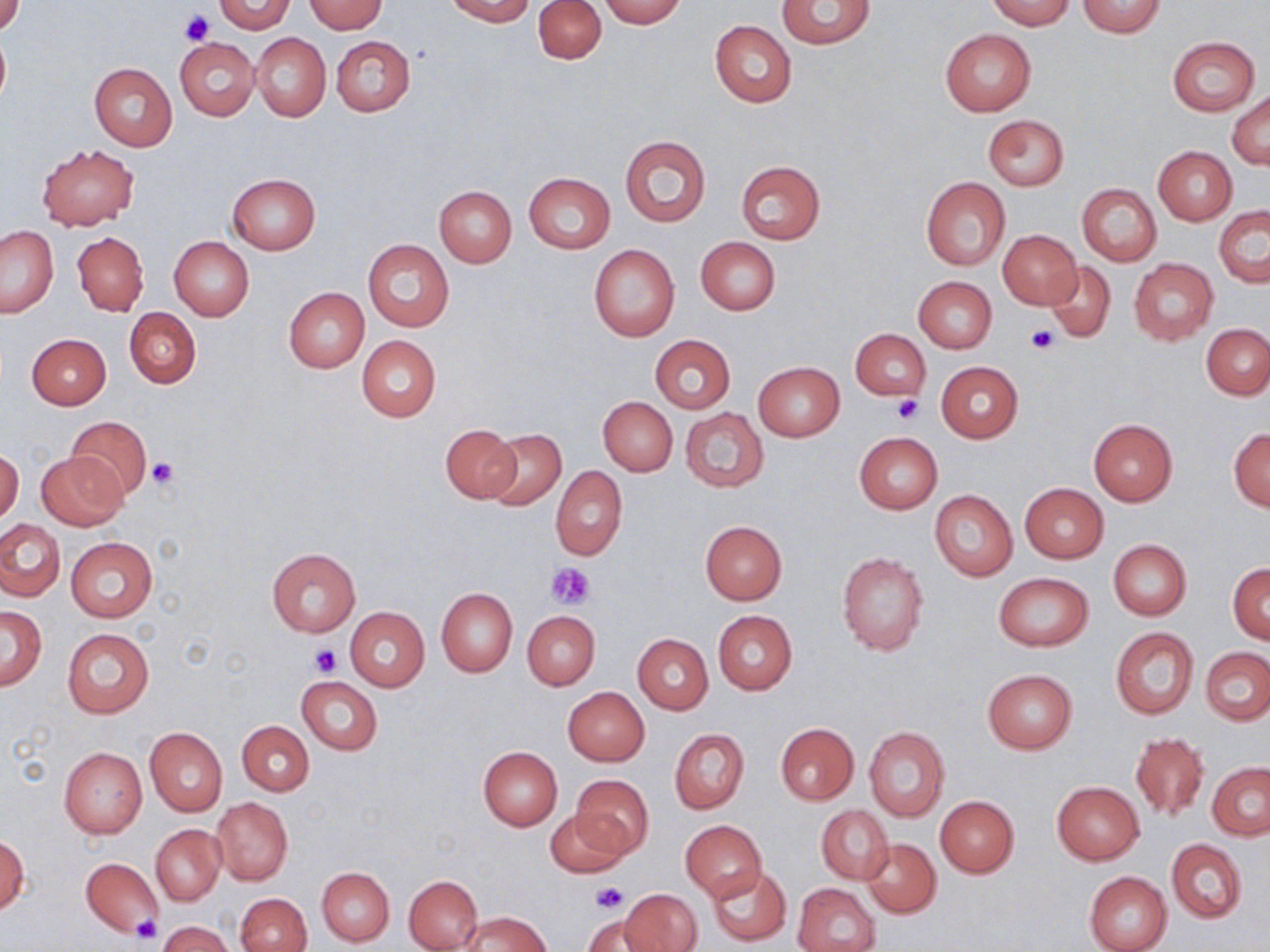
slide-level diagnosis = negative for blood parasites
stain = May-Grünwald-Giemsa
image size = 1270×952 pixels
preparation = thin blood smear
platelet locations = approximate bounding boxes as named x1/y1/x2/y2 corners in pixels: (x1=181, y1=10, x2=213, y2=45), (x1=1027, y1=324, x2=1060, y2=353), (x1=890, y1=394, x2=923, y2=424), (x1=147, y1=457, x2=178, y2=489), (x1=548, y1=561, x2=596, y2=608), (x1=311, y1=645, x2=342, y2=676), (x1=591, y1=883, x2=626, y2=915), (x1=130, y1=916, x2=161, y2=946)
field of view = single
magnification = 1000x
modality = light microscopy
uninfected red blood cell locations = approximate bounding boxes as named x1/y1/x2/y2 corners in pixels: (x1=0, y1=0, x2=26, y2=35), (x1=215, y1=0, x2=294, y2=33), (x1=445, y1=0, x2=534, y2=24), (x1=534, y1=0, x2=607, y2=64), (x1=776, y1=0, x2=875, y2=49), (x1=986, y1=0, x2=1075, y2=29), (x1=1077, y1=0, x2=1166, y2=39), (x1=306, y1=1, x2=386, y2=34), (x1=597, y1=1, x2=688, y2=25), (x1=710, y1=21, x2=796, y2=108), (x1=0, y1=28, x2=10, y2=108), (x1=941, y1=29, x2=1035, y2=117), (x1=253, y1=32, x2=331, y2=122), (x1=1167, y1=35, x2=1260, y2=115), (x1=332, y1=36, x2=415, y2=117), (x1=176, y1=37, x2=260, y2=120), (x1=89, y1=61, x2=178, y2=151), (x1=1228, y1=90, x2=1270, y2=168), (x1=983, y1=115, x2=1068, y2=190), (x1=620, y1=136, x2=711, y2=227), (x1=37, y1=143, x2=139, y2=230), (x1=1153, y1=147, x2=1237, y2=225), (x1=735, y1=160, x2=827, y2=245), (x1=523, y1=172, x2=615, y2=254), (x1=227, y1=174, x2=320, y2=254), (x1=922, y1=177, x2=1010, y2=270), (x1=1077, y1=184, x2=1161, y2=265), (x1=434, y1=185, x2=516, y2=268), (x1=1214, y1=206, x2=1270, y2=287), (x1=1, y1=226, x2=58, y2=317), (x1=1000, y1=229, x2=1082, y2=310), (x1=73, y1=232, x2=148, y2=316), (x1=168, y1=236, x2=254, y2=320), (x1=696, y1=237, x2=780, y2=315), (x1=362, y1=239, x2=455, y2=332), (x1=589, y1=244, x2=680, y2=342), (x1=1129, y1=258, x2=1217, y2=344), (x1=1044, y1=262, x2=1115, y2=343), (x1=915, y1=276, x2=996, y2=353), (x1=284, y1=287, x2=369, y2=373), (x1=124, y1=308, x2=200, y2=389), (x1=1202, y1=324, x2=1270, y2=399), (x1=851, y1=329, x2=929, y2=401), (x1=25, y1=333, x2=111, y2=409), (x1=649, y1=334, x2=736, y2=414), (x1=357, y1=335, x2=441, y2=422), (x1=936, y1=361, x2=1022, y2=442), (x1=753, y1=362, x2=843, y2=441), (x1=597, y1=396, x2=678, y2=476), (x1=681, y1=408, x2=768, y2=493), (x1=67, y1=415, x2=152, y2=499), (x1=1088, y1=418, x2=1177, y2=505), (x1=440, y1=425, x2=521, y2=503), (x1=1229, y1=428, x2=1270, y2=511), (x1=484, y1=429, x2=566, y2=510), (x1=853, y1=432, x2=942, y2=514), (x1=0, y1=449, x2=23, y2=526), (x1=37, y1=451, x2=128, y2=531), (x1=551, y1=466, x2=627, y2=560), (x1=1020, y1=482, x2=1108, y2=563), (x1=929, y1=490, x2=1018, y2=581), (x1=0, y1=518, x2=64, y2=600), (x1=699, y1=521, x2=787, y2=604), (x1=65, y1=537, x2=158, y2=623), (x1=1108, y1=539, x2=1192, y2=620), (x1=266, y1=548, x2=362, y2=636), (x1=836, y1=553, x2=927, y2=655), (x1=1228, y1=563, x2=1270, y2=644), (x1=993, y1=572, x2=1094, y2=651), (x1=437, y1=588, x2=518, y2=676), (x1=0, y1=607, x2=46, y2=689), (x1=345, y1=607, x2=429, y2=692), (x1=523, y1=611, x2=600, y2=690), (x1=713, y1=611, x2=796, y2=694), (x1=1110, y1=626, x2=1198, y2=719), (x1=62, y1=627, x2=153, y2=719), (x1=632, y1=633, x2=713, y2=714), (x1=1201, y1=647, x2=1269, y2=725), (x1=982, y1=668, x2=1078, y2=753), (x1=297, y1=676, x2=382, y2=755), (x1=564, y1=687, x2=649, y2=765), (x1=238, y1=721, x2=314, y2=795), (x1=775, y1=723, x2=858, y2=803), (x1=144, y1=726, x2=227, y2=817), (x1=863, y1=726, x2=950, y2=821), (x1=669, y1=728, x2=750, y2=813), (x1=1131, y1=732, x2=1209, y2=823), (x1=59, y1=747, x2=147, y2=838), (x1=477, y1=747, x2=562, y2=830), (x1=1207, y1=762, x2=1269, y2=840), (x1=571, y1=773, x2=654, y2=859), (x1=1052, y1=782, x2=1144, y2=865), (x1=935, y1=796, x2=1019, y2=877), (x1=212, y1=797, x2=293, y2=885), (x1=817, y1=806, x2=894, y2=884), (x1=544, y1=808, x2=631, y2=879), (x1=680, y1=821, x2=767, y2=899), (x1=150, y1=824, x2=225, y2=905), (x1=1, y1=835, x2=29, y2=917), (x1=861, y1=836, x2=941, y2=918), (x1=1166, y1=838, x2=1247, y2=924), (x1=81, y1=857, x2=163, y2=936), (x1=707, y1=865, x2=791, y2=946), (x1=317, y1=867, x2=394, y2=947), (x1=1083, y1=871, x2=1172, y2=952), (x1=403, y1=874, x2=484, y2=951), (x1=793, y1=883, x2=880, y2=952), (x1=622, y1=887, x2=703, y2=952), (x1=236, y1=893, x2=312, y2=952), (x1=460, y1=912, x2=550, y2=952), (x1=582, y1=915, x2=657, y2=951), (x1=158, y1=921, x2=234, y2=952)